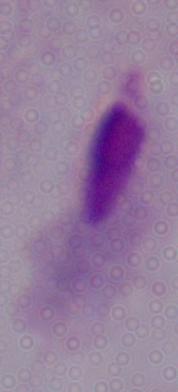
Photomicrograph. 1000x magnification. A trichomonad is seen.